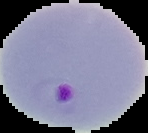
Malaria status: parasitized. From a thin blood film. Image is 148×133 pixels. Segmented cell region on a black background.